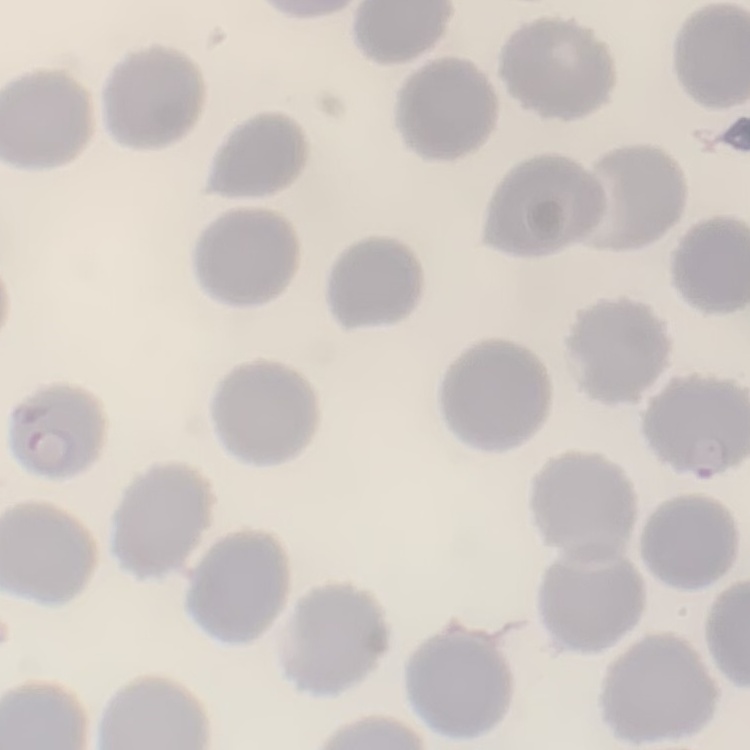

erythrocyte morphology = no rouleaux formation
preparation = thin blood film
image type = one tile cut from a larger photomicrograph
stain = Field's or Giemsa